Point out every Plasmodium parasite.
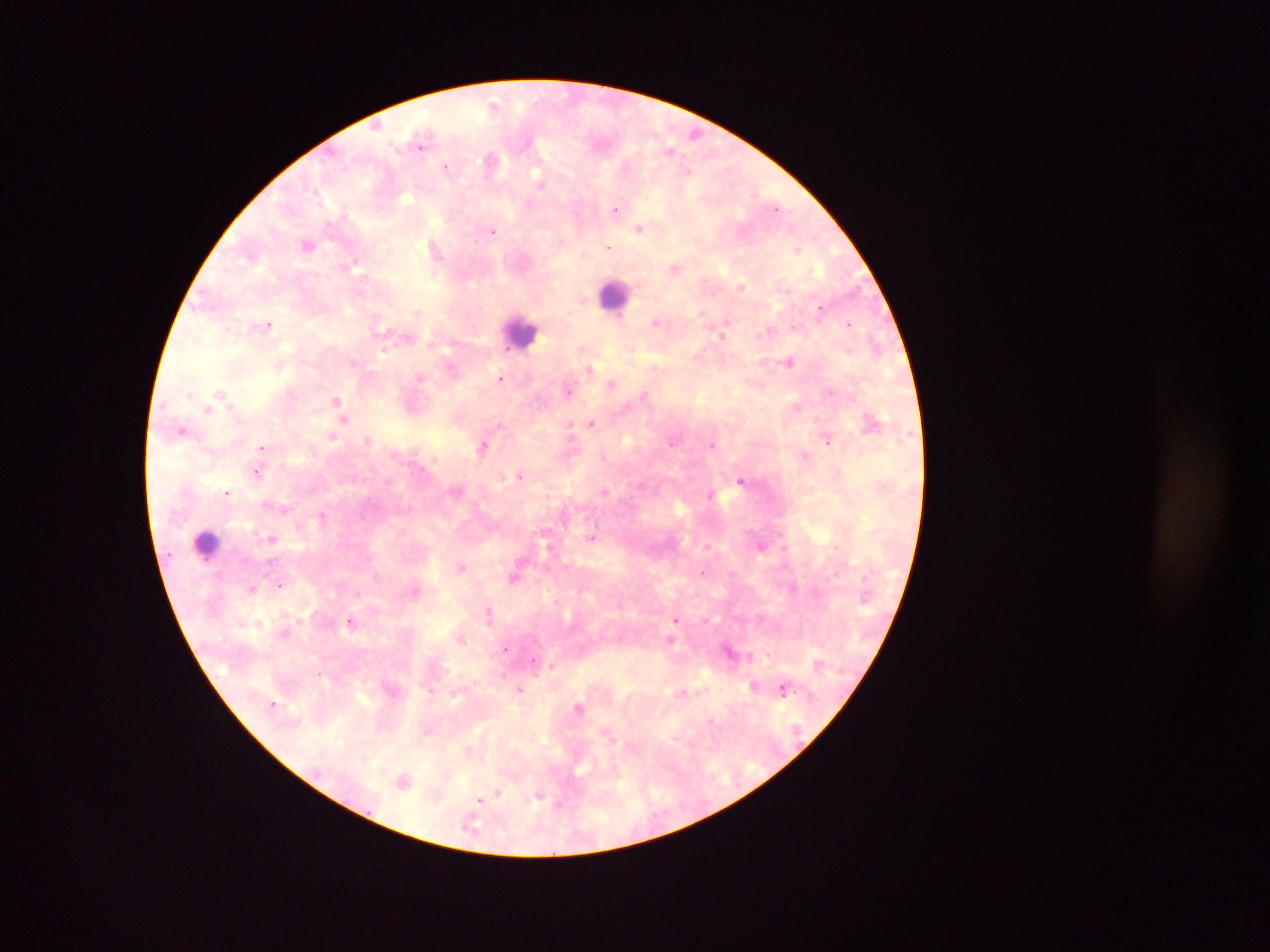
Approximate centers as {x, y} in pixels.
Plasmodium parasites: {493, 104}, {695, 133}, {421, 145}, {669, 150}, {491, 160}, {446, 166}, {688, 171}, {539, 182}, {776, 208}, {616, 209}, {639, 229}, {493, 231}, {308, 243}, {609, 247}, {797, 251}, {354, 263}, {675, 268}, {742, 287}, {821, 308}, {656, 322}, {849, 324}, {268, 325}, {769, 330}, {721, 334}, {875, 345}, {789, 361}, {589, 369}, {420, 377}, {500, 379}, {611, 383}, {569, 391}, {220, 392}, {190, 395}, {643, 395}, {336, 401}, {796, 407}, {208, 410}, {344, 419}, {592, 422}, {499, 424}, {182, 429}, {569, 429}, {332, 435}, {367, 439}, {827, 441}, {671, 443}, {712, 445}, {261, 447}, {483, 447}, {256, 473}, {520, 476}, {741, 480}, {605, 492}, {227, 493}, {710, 494}, {323, 515}, {591, 537}, {271, 538}, {461, 567}, {702, 572}, {514, 577}, {280, 585}, {253, 589}, {489, 612}, {676, 619}, {350, 622}, {461, 639}, {506, 648}, {534, 662}, {553, 665}, {754, 686}, {519, 689}, {783, 689}, {579, 708}, {404, 781}, {497, 793}, {538, 796}, {480, 800}.

Leukocyte locations: {615, 296}, {521, 332}, {207, 544}. Thick blood smear. Collected in Ghana. Mobile-phone photograph taken through the microscope. One field of view. Image is 1270×952 pixels.